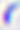
400x magnification. Micrograph. Toxoplasma gondii is shown.